Name the parasite shown.
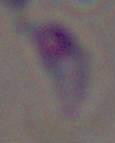

This is Toxoplasma gondii.

modality: photomicrograph
magnification: 1000x